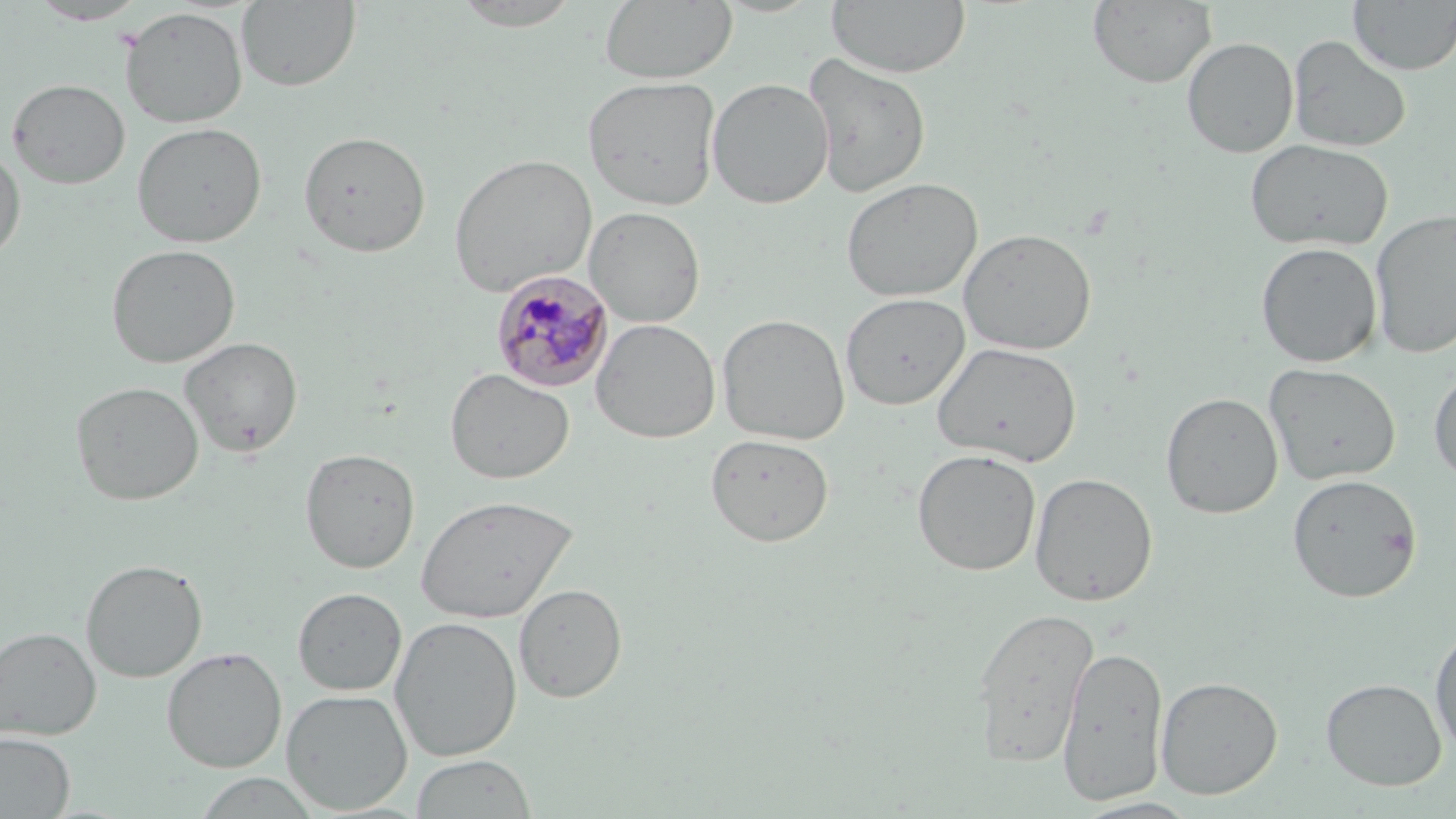 Approximate bounding boxes as (x1,y1)-(x2,y2) corner pairs in pixels. Uninfected red blood cell locations: (237,0)-(361,92), (448,0)-(586,31), (599,0)-(737,84), (827,0)-(971,79), (27,1)-(151,25), (1087,1)-(1216,88), (1348,1)-(1456,75), (120,7)-(248,128), (1287,35)-(1412,153), (1181,36)-(1299,158), (802,53)-(932,199), (582,75)-(721,210), (7,78)-(130,189), (706,78)-(834,209), (131,122)-(267,248), (298,130)-(431,257), (1244,139)-(1394,252), (0,147)-(26,262), (448,153)-(597,296), (841,177)-(983,303), (584,206)-(706,328), (1370,209)-(1456,359), (958,228)-(1097,356), (1255,241)-(1383,368), (106,243)-(241,368), (840,292)-(969,410), (716,313)-(850,445), (591,318)-(721,444), (179,336)-(303,457), (931,342)-(1082,467), (1264,363)-(1401,486), (1428,364)-(1456,486), (445,368)-(574,485), (70,381)-(204,506), (1160,392)-(1284,519), (705,433)-(835,547), (300,447)-(420,574), (912,449)-(1041,576), (1029,472)-(1157,606), (1287,473)-(1422,602), (415,494)-(578,624), (80,559)-(207,683), (514,583)-(627,703), (293,587)-(407,695), (970,606)-(1098,766), (389,616)-(522,761), (1429,622)-(1456,758), (0,626)-(102,741), (1056,644)-(1168,806), (162,647)-(287,773), (1156,676)-(1283,799), (1320,677)-(1447,791), (281,689)-(413,814), (1,732)-(75,817), (410,753)-(538,818), (193,773)-(322,818), (1072,795)-(1202,818). Plasmodium malariae-infected red blood cell locations: (491,270)-(614,393). Slide-level diagnosis: Plasmodium malariae. Single field of view. 1000x magnification. Optical microscopy. May-Grünwald-Giemsa-stained preparation. Image is 1456×819 pixels. Thin blood smear.